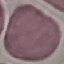 Result: no malaria parasites seen. Cell patch, automatically extracted from a larger field of view and resized to 64 × 64 pixels. Giemsa stain. Thin blood film. Photographed with a smartphone camera at the microscope eyepiece.